Classify this cell by malaria status.
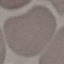
It is uninfected.

Summary:
  - Capture: smartphone camera at the microscope eyepiece
  - Image type: cell patch, automatically extracted from a larger field of view and resized to 64 × 64 pixels
  - Preparation: thin blood smear
  - Stain: Giemsa